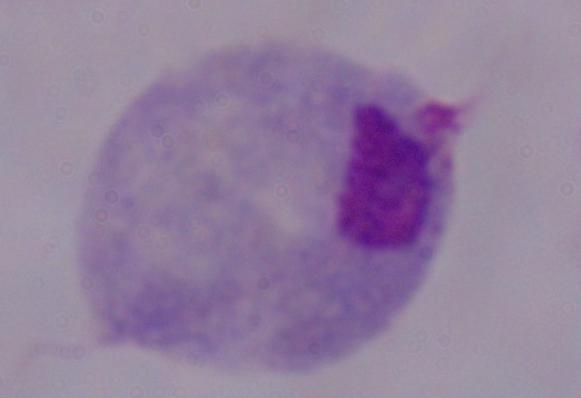

Summary:
  - Magnification: 1000x
  - Identification: trichomonad
  - Modality: micrograph